State which cell type is depicted.
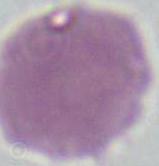

An erythrocyte.

Micrograph. Captured at 1000x magnification.